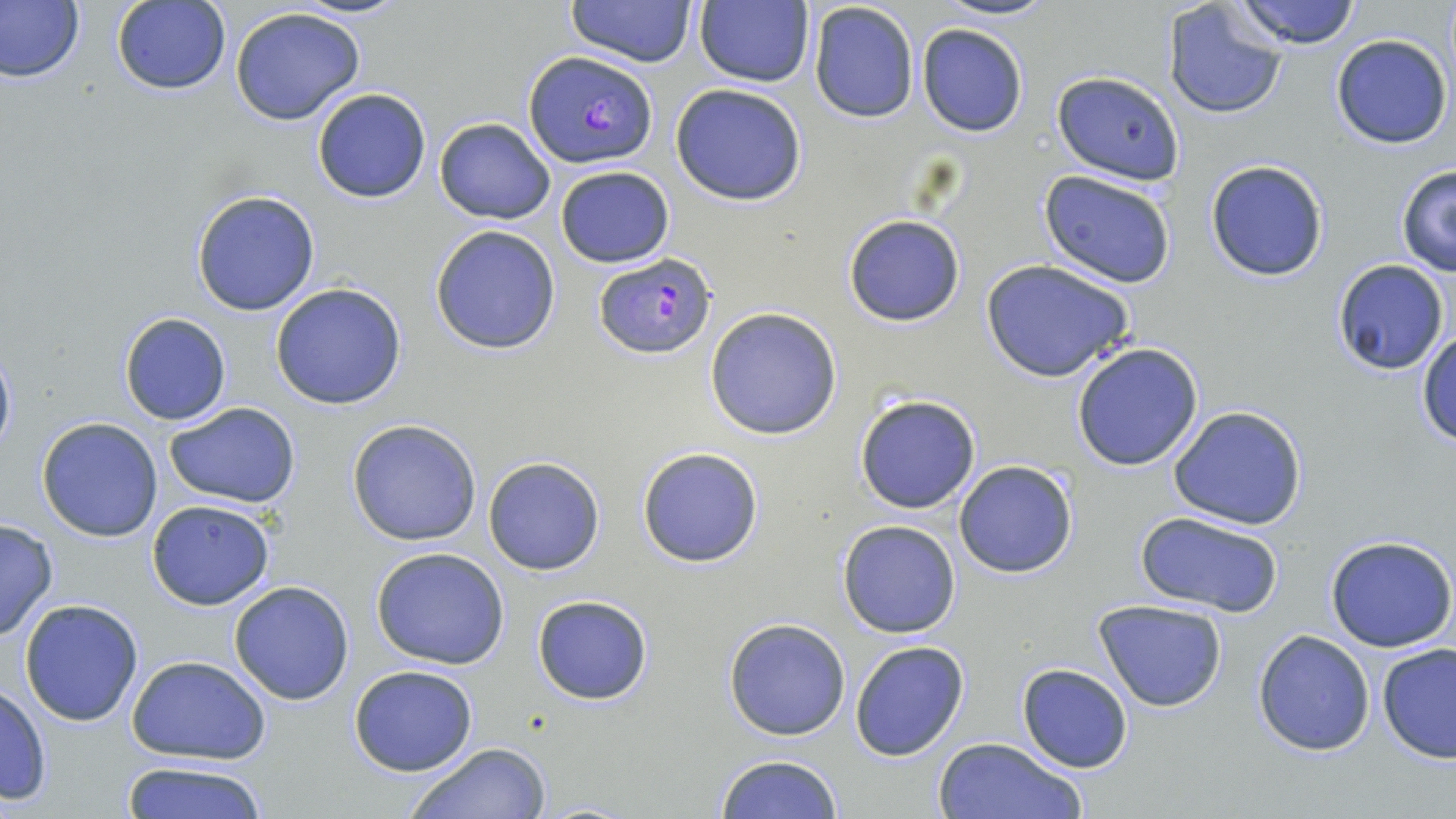

Approximate bounding boxes as (x1,y1)-(x2,y2) corner pairs in pixels. Uninfected red blood cell locations: (292,0)-(407,21), (568,0)-(698,68), (939,0)-(1056,22), (1233,0)-(1364,49), (0,1)-(84,84), (111,1)-(231,96), (697,1)-(812,87), (808,2)-(920,122), (1163,3)-(1288,121), (228,8)-(368,127), (916,24)-(1028,137), (1331,33)-(1453,150), (1053,72)-(1184,182), (670,83)-(808,207), (312,87)-(432,203), (434,117)-(556,225), (1203,159)-(1330,283), (1394,164)-(1456,277), (554,166)-(674,268), (1039,169)-(1177,287), (191,189)-(322,316), (843,213)-(966,328), (429,225)-(563,354), (1332,257)-(1449,375), (980,260)-(1135,382), (270,282)-(407,411), (704,307)-(843,440), (119,313)-(231,426), (1415,329)-(1456,445), (0,337)-(16,465), (1071,342)-(1204,471), (853,392)-(983,515), (165,403)-(300,508), (1168,405)-(1309,531), (38,419)-(163,541), (347,419)-(481,546), (637,447)-(764,567), (481,456)-(606,575), (953,461)-(1078,579), (146,499)-(276,611), (1136,512)-(1283,619), (0,519)-(59,642), (838,519)-(962,638), (1325,535)-(1456,652), (371,546)-(510,669), (228,581)-(355,706), (532,594)-(654,706), (19,599)-(145,725), (1093,600)-(1228,713), (723,617)-(852,740), (1253,629)-(1375,756), (850,640)-(971,762), (1376,643)-(1456,763), (128,654)-(272,763), (1017,663)-(1133,773), (349,664)-(478,775), (0,684)-(52,804), (931,736)-(1084,819), (403,741)-(554,819), (714,753)-(843,819), (119,760)-(271,819). Plasmodium falciparum-infected red blood cell locations: (524,52)-(658,169), (592,251)-(718,360). Slide-level diagnosis: Plasmodium falciparum. Thin blood smear. Image is 1456×819 pixels. Single field of view. Captured at 1000x magnification. Light microscopy. May-Grünwald-Giemsa-stained preparation.